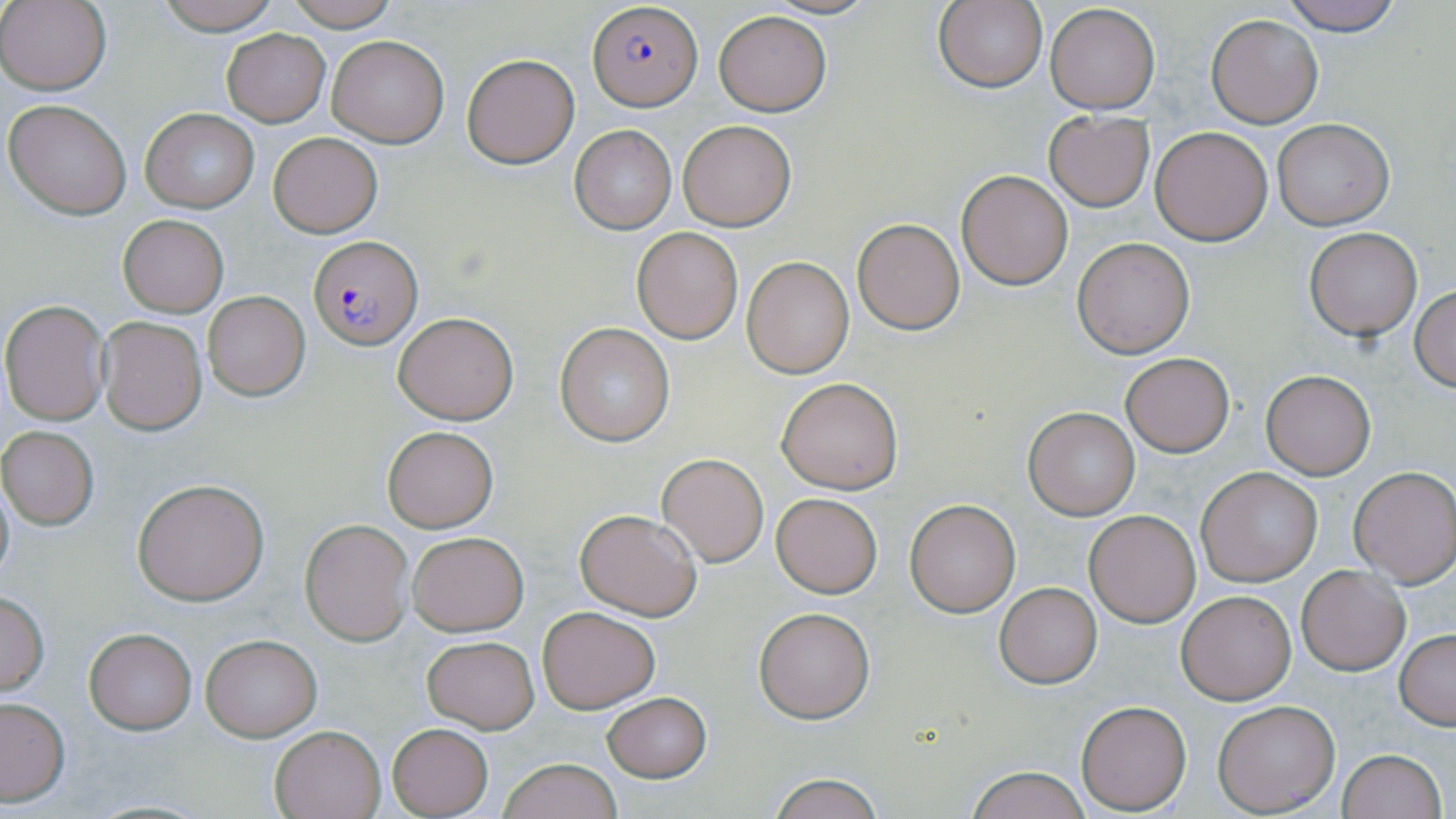

{
  "slide_level_diagnosis": "Plasmodium falciparum",
  "preparation": "thin blood film",
  "magnification": "1000x",
  "uninfected_red_blood_cell_locations": "approximate bounding boxes as (x1,y1)-(x2,y2) corner pairs in pixels: (155,0)-(283,34), (284,0)-(401,29), (756,0)-(886,18), (935,0)-(1049,93), (1276,0)-(1407,34), (0,1)-(110,93), (1043,2)-(1161,113), (713,10)-(831,116), (1206,13)-(1324,127), (222,30)-(330,126), (326,35)-(449,148), (462,53)-(578,168), (5,98)-(132,219), (141,108)-(259,214), (1043,111)-(1154,211), (1272,119)-(1394,230), (676,120)-(796,231), (568,124)-(677,235), (1150,126)-(1272,245), (267,132)-(383,238), (956,170)-(1073,291), (118,215)-(227,315), (851,217)-(966,335), (632,227)-(743,343), (1305,228)-(1421,340), (1072,237)-(1195,358), (742,257)-(854,378), (1410,286)-(1456,392), (203,291)-(311,401), (1,299)-(112,426), (393,312)-(519,424), (97,314)-(207,434), (554,323)-(676,447), (1121,353)-(1234,457), (1259,370)-(1376,479), (776,376)-(903,494), (1024,407)-(1142,519), (383,426)-(497,531), (1,427)-(100,530), (657,453)-(768,566), (1347,465)-(1456,587), (1196,467)-(1323,586), (0,473)-(15,593), (132,479)-(270,605), (771,492)-(883,597), (906,498)-(1019,617), (575,508)-(703,620), (1083,509)-(1200,628), (301,519)-(413,644), (406,530)-(528,636), (1297,565)-(1410,675), (995,582)-(1102,687), (0,589)-(49,698), (1177,590)-(1296,704), (538,606)-(660,713), (753,606)-(874,722), (84,628)-(198,733), (1396,629)-(1456,730), (199,634)-(321,741), (422,635)-(539,733), (602,691)-(712,782), (0,697)-(71,806), (1076,700)-(1191,814), (1213,700)-(1339,816), (387,723)-(493,817), (270,725)-(385,818), (1336,748)-(1447,819), (498,757)-(622,819), (965,765)-(1093,819), (765,771)-(885,818)",
  "plasmodium_falciparum_infected_red_blood_cell_locations": "approximate bounding boxes as (x1,y1)-(x2,y2) corner pairs in pixels: (587,3)-(700,110), (308,236)-(422,350)",
  "stain": "May-Grünwald-Giemsa",
  "image_size": "1456×819 pixels",
  "modality": "light microscopy",
  "field_of_view": "one of a larger specimen"
}